Point out each Plasmodium parasite.
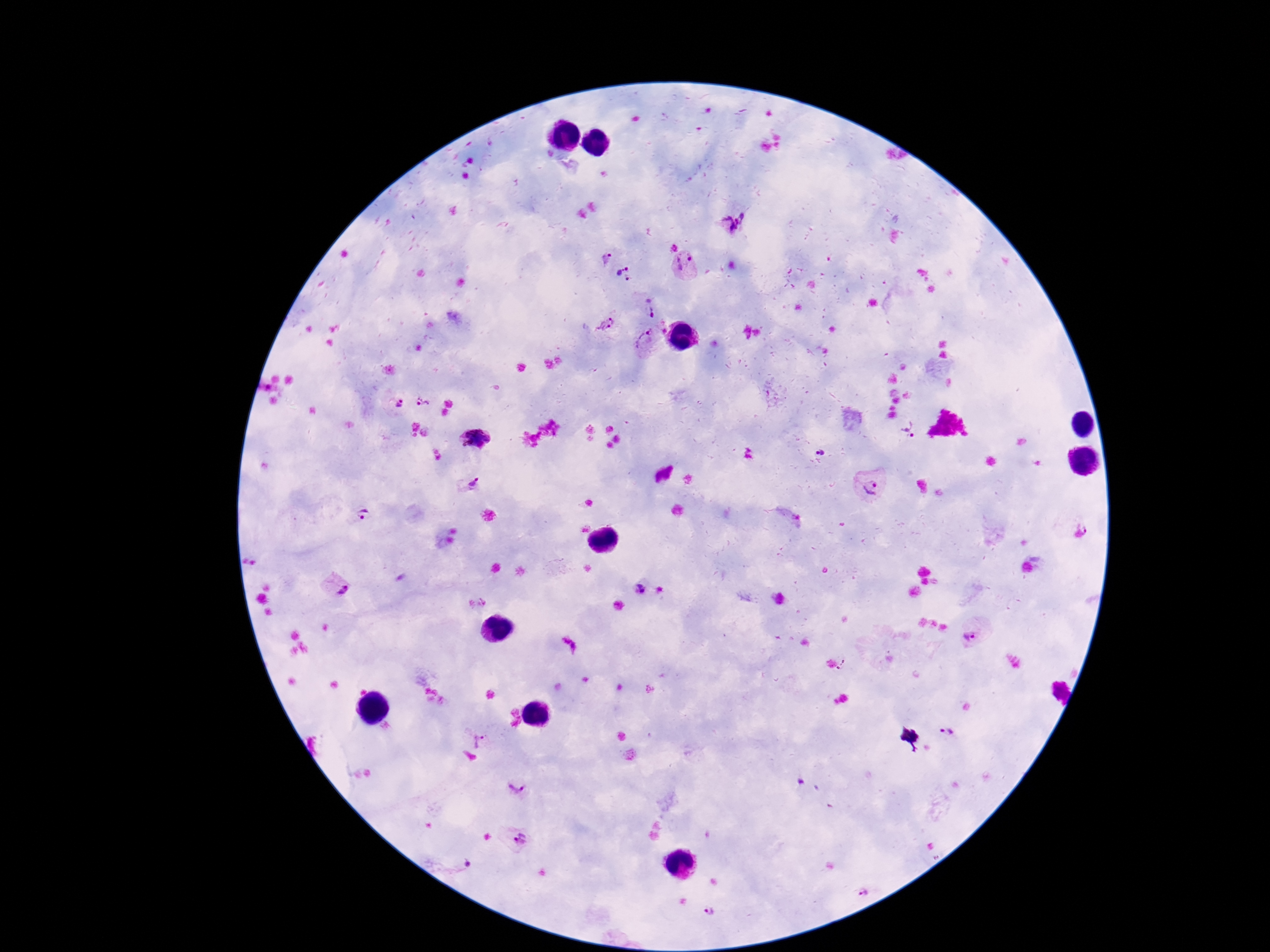
Approximate centers as [x, y] in pixels.
Plasmodium parasites: [735, 222], [600, 256], [685, 265], [626, 277], [651, 306], [606, 323], [644, 340], [423, 402], [400, 403], [909, 428], [477, 438], [819, 451], [471, 484], [871, 489], [359, 513], [1085, 525], [640, 587], [340, 588], [972, 636], [947, 731], [479, 740], [518, 786], [518, 840], [861, 891], [711, 912].

Summary:
  - Image size: 1270×952 pixels
  - Magnification: 100x
  - Stain: Giemsa
  - Field of view: single
  - Capture: smartphone camera through the microscope eyepiece
  - Patient malaria status: infected
  - Preparation: thick blood smear